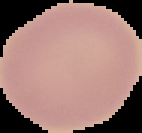

Cell region segmented out of the field of view; the surrounding area is masked to black. From a thin blood film. Image is 142×133 pixels. Result: no Plasmodium parasites seen.